Report the malaria status.
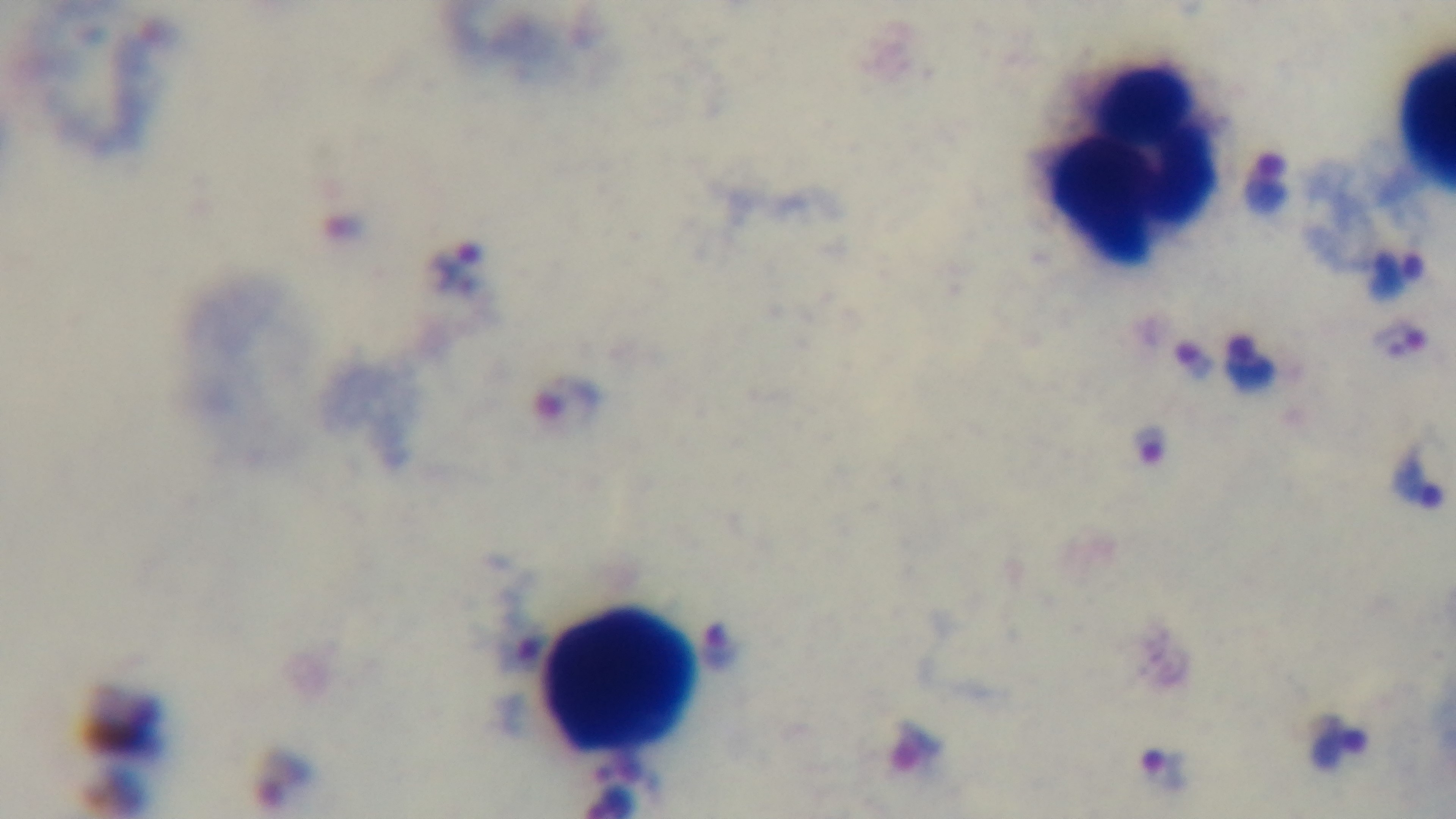
It is infected.

field_of_view: one from the slide
preparation: thick smear
modality: light microscopy
objective: 100x oil immersion
capture: mounted 4K digital camera
stain: Giemsa